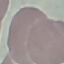
result = negative for malaria parasites
image type = automatically extracted cell patch, resized to 64 × 64 pixels
preparation = thin smear
capture = smartphone camera at the microscope eyepiece
stain = Giemsa